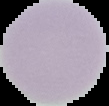

Result: negative for Plasmodium parasites. Cell region segmented out of the field of view; the surrounding area is masked to black. From a thin blood film. Image is 109×106 pixels.